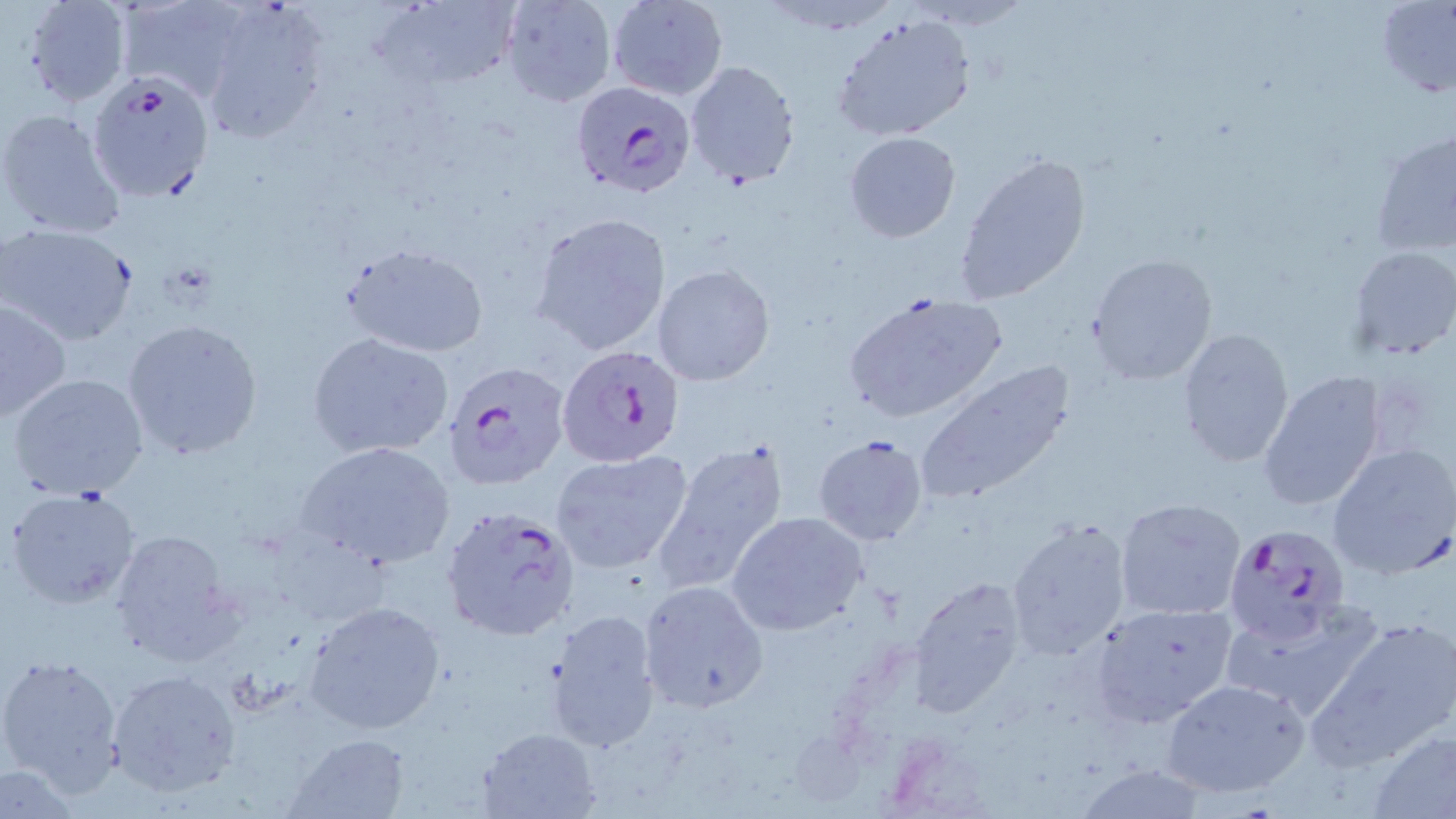
Summary:
  - Coordinate format: approximate bounding boxes as (x1, y1, x2, y2) in pixels
  - Plasmodium falciparum-infected red blood cell locations: (85, 70, 217, 204), (571, 81, 695, 196), (556, 340, 686, 470), (441, 362, 569, 489), (440, 505, 579, 642), (1224, 524, 1352, 644)
  - Uninfected red blood cell locations: (19, 0, 135, 107), (120, 0, 259, 103), (378, 0, 519, 91), (500, 0, 617, 107), (606, 0, 727, 100), (1376, 1, 1456, 96), (197, 2, 332, 144), (829, 10, 979, 144), (684, 59, 802, 187), (0, 106, 127, 242), (1369, 128, 1456, 263), (842, 131, 961, 242), (953, 152, 1093, 304), (531, 212, 671, 357), (1, 223, 139, 346), (344, 244, 489, 359), (1350, 245, 1456, 359), (1086, 253, 1217, 385), (654, 265, 775, 386), (843, 291, 1004, 421), (1, 299, 72, 421), (121, 316, 265, 461), (1175, 327, 1294, 470), (306, 331, 454, 460), (912, 360, 1078, 506), (1256, 369, 1388, 512), (7, 373, 150, 500), (813, 434, 929, 547), (651, 439, 792, 595), (296, 440, 456, 570), (1326, 443, 1456, 579), (549, 449, 695, 577), (5, 487, 144, 610), (1115, 498, 1246, 620), (726, 512, 869, 635), (1006, 517, 1133, 661), (106, 526, 245, 666), (907, 574, 1030, 716), (639, 581, 766, 710), (1218, 599, 1384, 724), (304, 600, 447, 736), (1088, 602, 1238, 728), (545, 608, 661, 752), (1313, 614, 1456, 766), (0, 650, 126, 798), (106, 669, 240, 796), (1161, 677, 1310, 798), (479, 726, 602, 817), (1369, 728, 1455, 816), (284, 732, 409, 816), (0, 762, 85, 816), (1073, 763, 1210, 818)
  - Slide-level diagnosis: Plasmodium falciparum
  - Image size: 1456×819 pixels
  - Stain: May-Grünwald-Giemsa
  - Field of view: single
  - Preparation: thin blood film
  - Modality: optical microscopy
  - Magnification: 1000x